Name the cell type shown.
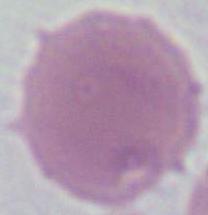
An erythrocyte.

modality: photomicrograph
magnification: 1000x